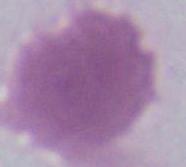

Summary:
  - Modality: micrograph
  - Identification: erythrocyte
  - Magnification: 1000x